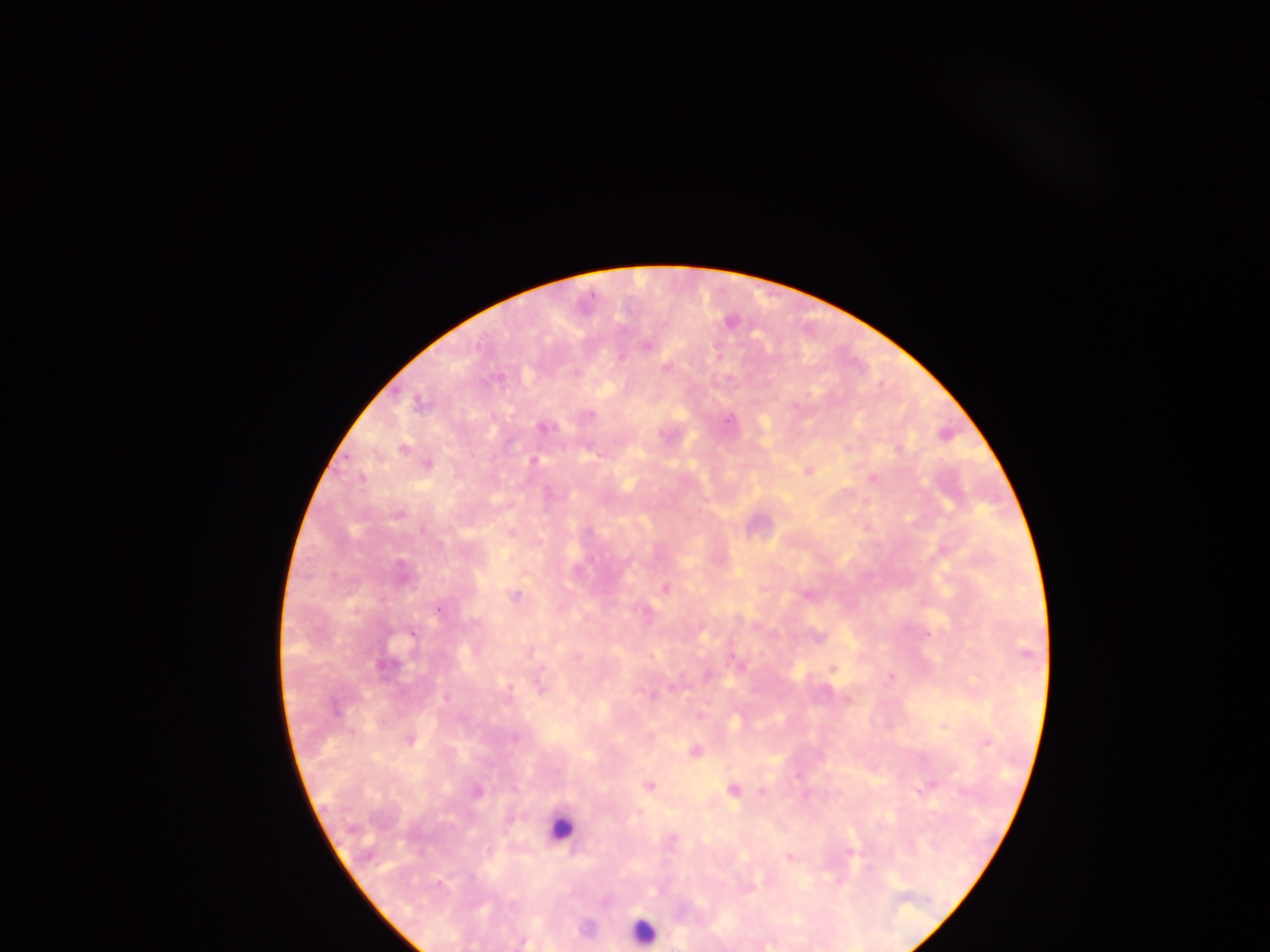
Approximate centers as [x, y] in pixels.
Summary:
  - Leukocyte locations: [559, 827], [642, 931]
  - Plasmodium parasite locations: [730, 322], [648, 346], [621, 358], [666, 368], [576, 373], [419, 404], [589, 414], [729, 420], [543, 428], [402, 448], [898, 450], [535, 461], [428, 465], [808, 471], [873, 477], [361, 478], [398, 515], [913, 522], [423, 530], [589, 531], [402, 566], [665, 588], [515, 595], [806, 595], [438, 609], [756, 627], [701, 632], [411, 635], [1025, 651], [577, 657], [739, 664], [384, 665], [833, 669], [707, 675], [891, 677], [541, 686], [673, 687], [826, 692], [651, 694], [446, 698], [848, 700], [335, 708], [700, 715], [734, 721], [944, 727], [515, 738], [410, 740], [987, 743], [694, 750], [951, 770], [798, 776], [649, 786], [733, 790], [922, 790], [761, 791], [477, 792], [964, 793], [673, 839], [488, 850], [850, 851], [788, 857], [440, 884], [523, 942]
  - Image size: 1270×952 pixels
  - Preparation: thick blood film
  - Capture: mobile-phone photograph through a microscope
  - Country: Ghana
  - Field of view: single